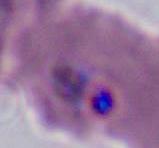

magnification = 400x or 1000x
modality = photomicrograph
identification = Plasmodium